Classify this cell by malaria status.
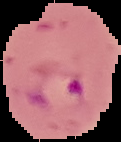

It is parasitized.

Summary:
  - Image size: 121×142 pixels
  - Image type: segmented cell region with the area outside set to black
  - Preparation: thin blood film